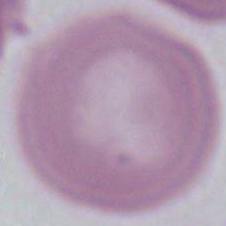

Summary:
  - Identification: red blood cell
  - Magnification: 1000x
  - Modality: photomicrograph